Locate and identify every blood parasite.
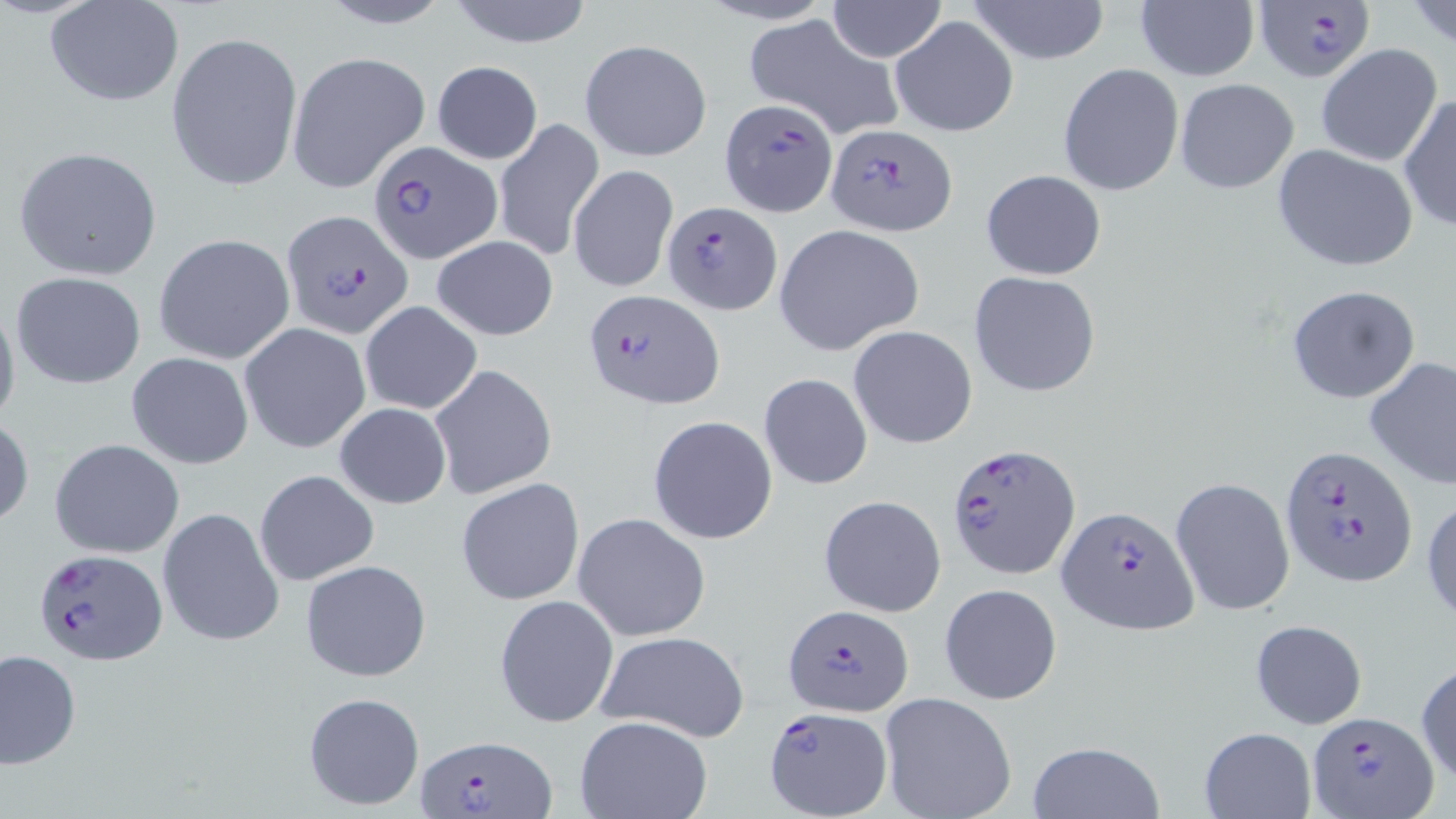
Approximate bounding boxes as [x1, y1, x2, y2] in pixels.
Plasmodium falciparum-infected red blood cells: [1252, 2, 1377, 83], [720, 98, 838, 218], [824, 124, 956, 235], [371, 139, 503, 263], [660, 198, 780, 312], [282, 210, 411, 337], [585, 289, 722, 410], [947, 442, 1077, 579], [1281, 444, 1417, 588], [1057, 504, 1199, 634], [31, 547, 167, 664], [783, 605, 915, 716], [765, 708, 892, 816], [1308, 711, 1438, 819], [416, 734, 555, 818].
No Plasmodium ovale, Plasmodium malariae, Plasmodium vivax, Babesia divergens, or Trypanosoma brucei observed.

Summary:
  - Uninfected red blood cell locations: [312, 0, 459, 31], [441, 0, 599, 48], [827, 0, 947, 61], [965, 0, 1111, 65], [1408, 0, 1456, 52], [1135, 1, 1260, 83], [44, 2, 186, 109], [891, 15, 1018, 136], [743, 16, 903, 139], [166, 29, 302, 194], [580, 39, 709, 161], [1316, 44, 1443, 167], [287, 51, 429, 193], [431, 61, 543, 165], [1057, 63, 1184, 196], [1174, 78, 1299, 195], [1399, 94, 1456, 232], [495, 119, 602, 263], [1272, 145, 1418, 272], [13, 146, 162, 280], [569, 163, 678, 293], [980, 169, 1107, 280], [773, 224, 924, 355], [153, 234, 295, 364], [431, 235, 559, 340], [11, 270, 147, 389], [968, 270, 1101, 397], [1285, 284, 1421, 404], [0, 296, 20, 435], [359, 301, 483, 416], [239, 323, 370, 453], [848, 326, 978, 450], [126, 351, 254, 467], [1364, 356, 1456, 489], [430, 365, 558, 497], [759, 374, 873, 489], [333, 401, 452, 509], [0, 415, 34, 530], [648, 416, 778, 544], [50, 439, 184, 556], [253, 469, 380, 586], [1170, 476, 1296, 619], [455, 478, 584, 606], [818, 494, 947, 618], [1423, 494, 1456, 626], [158, 507, 284, 647], [574, 512, 711, 640], [300, 558, 432, 683], [940, 583, 1062, 705], [494, 594, 618, 728], [1248, 618, 1368, 730], [596, 631, 751, 743], [2, 649, 80, 769], [1415, 661, 1456, 784], [302, 691, 426, 811], [879, 692, 1017, 819], [574, 716, 714, 819], [1199, 727, 1315, 817], [1026, 740, 1165, 819]
  - Slide-level diagnosis: Plasmodium falciparum
  - Stain: May-Grünwald-Giemsa
  - Image size: 1456×819 pixels
  - Magnification: 1000x
  - Preparation: thin blood film
  - Field of view: one of a larger specimen
  - Modality: optical microscopy